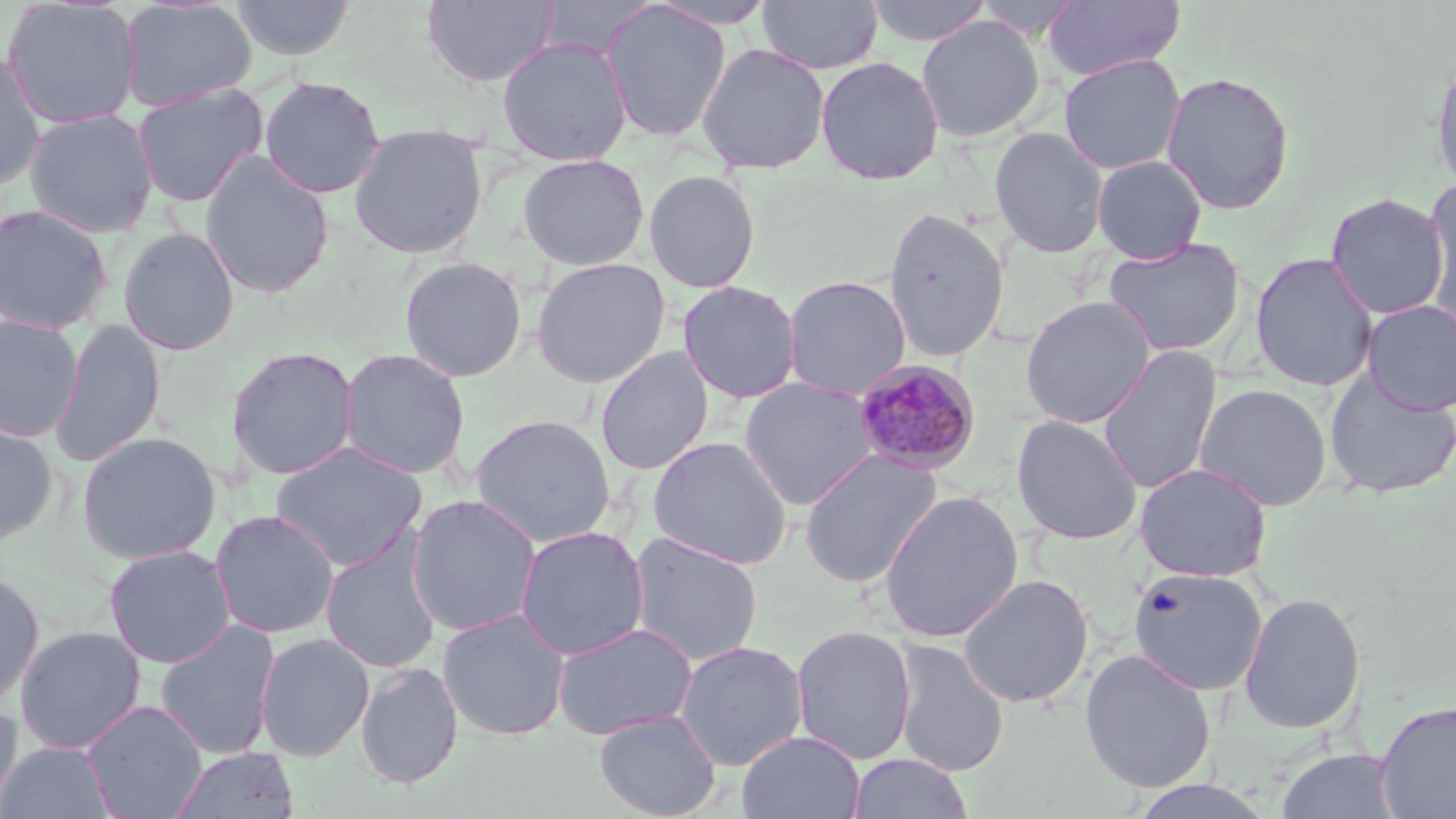 Approximate bounding boxes as (x1,y1)-(x2,y2) corner pairs in pixels. Uninfected red blood cell locations: (1,0)-(143,130), (231,0)-(355,61), (422,0)-(559,88), (647,0)-(779,29), (758,0)-(882,74), (863,0)-(995,46), (1043,0)-(1185,82), (120,1)-(256,112), (600,2)-(732,141), (915,15)-(1045,142), (496,36)-(633,166), (695,42)-(831,175), (0,51)-(45,192), (1058,53)-(1186,175), (815,55)-(945,185), (1430,55)-(1456,195), (1160,70)-(1295,215), (259,76)-(386,199), (131,82)-(268,206), (24,108)-(159,238), (347,122)-(489,259), (989,126)-(1109,258), (199,152)-(334,298), (517,152)-(650,271), (1091,155)-(1208,263), (643,169)-(761,293), (1421,181)-(1456,327), (1325,192)-(1451,320), (0,204)-(113,334), (882,207)-(1010,363), (0,215)-(240,339), (117,226)-(241,356), (1104,237)-(1246,357), (1249,252)-(1379,392), (399,255)-(528,382), (530,257)-(671,388), (782,275)-(912,401), (677,280)-(802,404), (1020,295)-(1157,429), (1361,300)-(1456,415), (0,314)-(84,442), (49,319)-(166,467), (1097,345)-(1222,495), (226,346)-(360,480), (595,346)-(715,476), (339,348)-(471,480), (1324,369)-(1456,498), (739,376)-(881,509), (1194,383)-(1332,511), (470,414)-(616,547), (1011,414)-(1144,545), (0,418)-(59,544), (77,431)-(221,565), (648,435)-(793,570), (269,441)-(428,572), (800,449)-(943,588), (1134,462)-(1273,581), (878,490)-(1024,643), (405,494)-(542,637), (210,509)-(340,639), (515,526)-(649,660), (628,531)-(764,666), (320,535)-(442,674), (104,544)-(236,668), (1128,566)-(1268,696), (0,569)-(44,710), (957,573)-(1094,709), (1238,592)-(1366,734), (437,608)-(571,741), (154,619)-(281,760), (551,621)-(698,740), (790,624)-(918,765), (14,625)-(147,754), (255,632)-(375,762), (890,638)-(1010,776), (674,640)-(809,772), (1079,648)-(1217,793), (356,660)-(464,789), (0,699)-(23,818), (81,699)-(208,818), (1374,700)-(1456,819), (594,709)-(722,819), (736,731)-(865,819), (1,740)-(114,818), (169,746)-(300,819), (1276,748)-(1402,818), (846,753)-(974,818). Plasmodium malariae-infected red blood cell locations: (853,360)-(982,476). Slide-level diagnosis: Plasmodium malariae. Captured at 1000x magnification. Optical microscopy. One field of a larger specimen. May-Grünwald-Giemsa stain. Thin blood smear. Image is 1456×819 pixels.